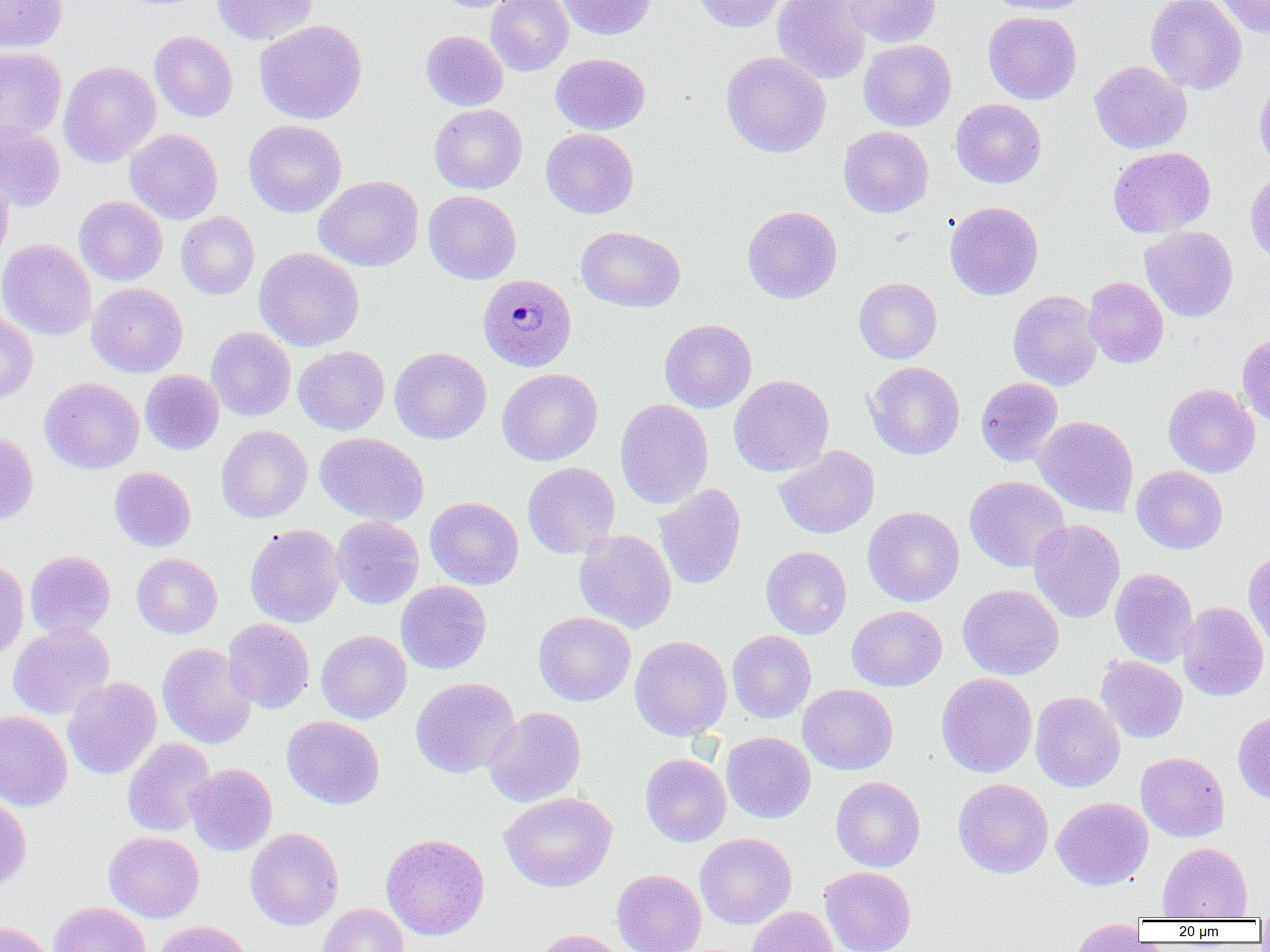 Approximate bounding boxes as (x1, y1, x2, y2) in pixels. Plasmodium malariae-infected red blood cell locations: (478, 274, 576, 371). Uninfected red blood cell locations: (0, 0, 67, 53), (212, 0, 318, 45), (435, 0, 523, 13), (486, 0, 573, 76), (556, 0, 655, 40), (693, 0, 788, 32), (772, 0, 871, 84), (842, 0, 940, 47), (985, 0, 1093, 15), (1146, 0, 1246, 94), (1215, 0, 1270, 39), (983, 11, 1082, 104), (255, 20, 367, 124), (149, 31, 238, 121), (421, 31, 508, 111), (858, 39, 957, 131), (0, 47, 67, 142), (721, 52, 831, 157), (551, 53, 650, 135), (1089, 60, 1191, 154), (59, 61, 161, 167), (1254, 75, 1270, 178), (950, 98, 1046, 188), (429, 104, 527, 194), (243, 119, 347, 218), (0, 120, 65, 212), (838, 126, 934, 217), (125, 129, 222, 224), (541, 129, 638, 218), (1108, 146, 1215, 238), (0, 170, 13, 266), (1245, 170, 1270, 266), (314, 176, 423, 271), (423, 190, 521, 284), (74, 196, 168, 285), (945, 201, 1043, 300), (742, 205, 842, 303), (176, 211, 259, 299), (576, 226, 685, 312), (1139, 226, 1238, 322), (0, 239, 96, 340), (254, 247, 363, 351), (1083, 277, 1169, 368), (854, 278, 942, 363), (87, 283, 187, 377), (1007, 290, 1103, 390), (0, 312, 38, 403), (659, 319, 756, 412), (206, 327, 296, 421), (1237, 334, 1270, 427), (293, 345, 389, 435), (390, 347, 491, 444), (866, 361, 964, 459), (497, 368, 602, 466), (140, 370, 224, 455), (728, 375, 834, 477), (40, 377, 144, 474), (975, 377, 1062, 466), (1163, 384, 1260, 477), (615, 399, 713, 509), (1033, 415, 1139, 516), (216, 425, 312, 522), (0, 431, 38, 525), (315, 432, 429, 526), (773, 444, 879, 538), (522, 462, 620, 558), (1131, 466, 1228, 554), (109, 467, 196, 552), (964, 476, 1071, 572), (654, 484, 746, 590), (425, 496, 524, 590), (863, 506, 964, 606), (331, 511, 525, 600), (332, 515, 424, 609), (1028, 519, 1125, 623), (245, 524, 345, 628), (574, 530, 677, 633), (761, 546, 851, 639), (1243, 549, 1270, 653), (25, 550, 115, 640), (132, 554, 222, 638), (0, 559, 29, 660), (1110, 568, 1198, 667), (396, 581, 491, 674), (957, 584, 1064, 680), (1178, 601, 1269, 701), (847, 605, 947, 691), (533, 612, 635, 706), (223, 618, 315, 713), (8, 622, 114, 720), (316, 630, 411, 723), (727, 630, 816, 722), (630, 635, 732, 740), (158, 643, 257, 748), (1096, 656, 1187, 743), (936, 673, 1037, 778), (63, 676, 161, 780), (410, 678, 519, 778), (798, 684, 898, 775), (1031, 691, 1125, 792), (484, 706, 586, 807), (1233, 710, 1270, 805), (0, 711, 72, 810), (282, 715, 384, 808), (721, 731, 816, 823), (122, 738, 216, 837), (1135, 752, 1230, 842), (640, 753, 731, 847), (186, 764, 277, 855), (831, 776, 925, 872), (953, 778, 1053, 878), (499, 792, 617, 892), (0, 793, 32, 890), (1052, 797, 1153, 890), (245, 828, 344, 931), (104, 831, 204, 922), (381, 833, 490, 940), (695, 833, 796, 929), (1157, 842, 1252, 920), (819, 866, 916, 952), (612, 869, 706, 952), (48, 901, 151, 952), (317, 903, 409, 952), (747, 906, 838, 952), (0, 920, 55, 952), (151, 920, 255, 952), (1069, 920, 1147, 951), (529, 928, 631, 952). Slide-level diagnosis: Plasmodium malariae. Light microscopy. Image is 1270×952 pixels. Captured at 1000x magnification. Thin blood smear. Single field of view.